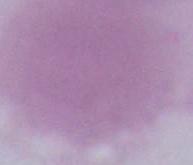
Summary:
  - Magnification: 1000x
  - Modality: micrograph
  - Identification: erythrocyte